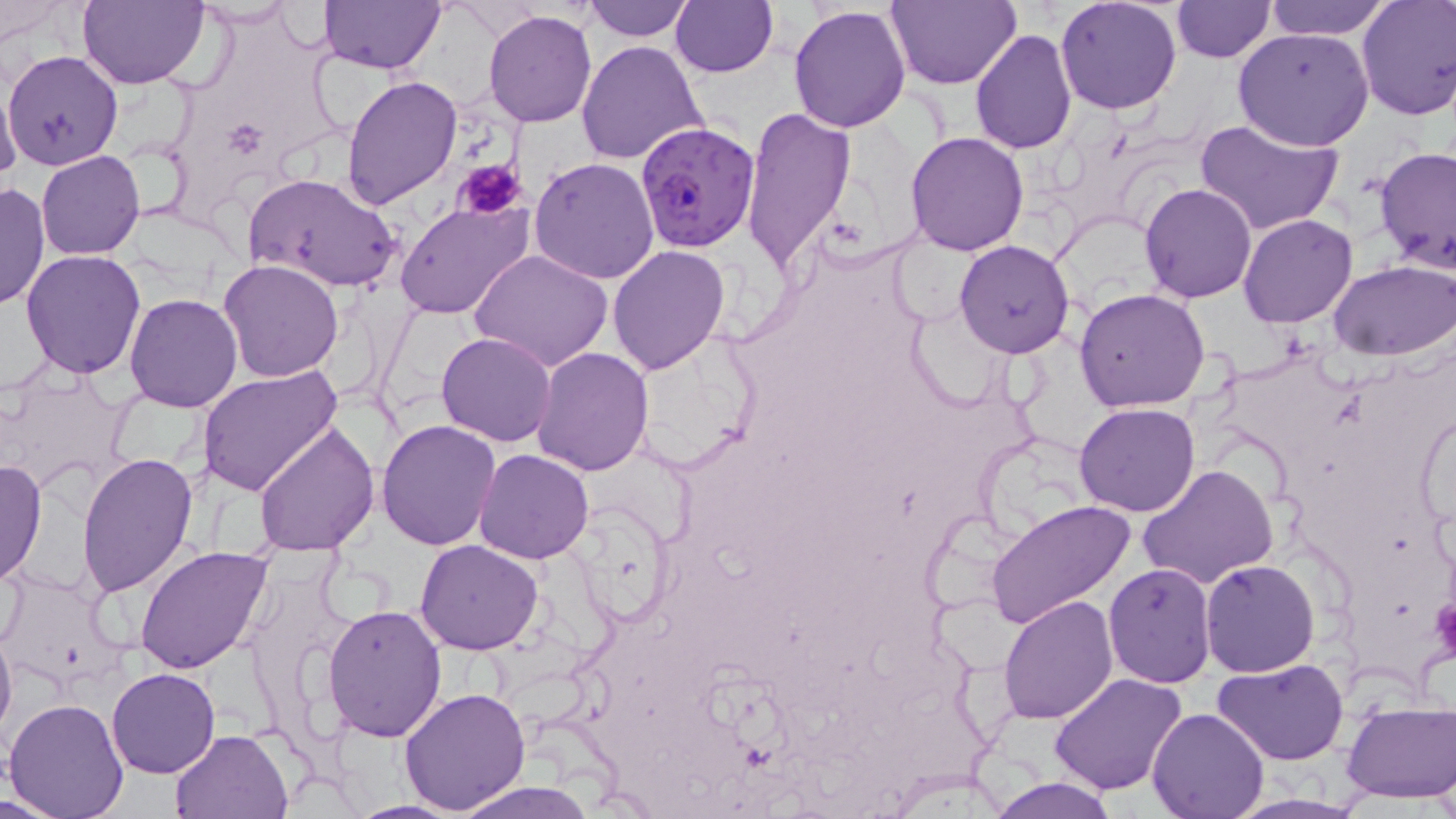

slide-level diagnosis = Plasmodium falciparum
field of view = single
stain = May-Grünwald-Giemsa
platelet locations = approximate bounding boxes as (x1, y1, x2, y2) in pixels: (453, 157, 528, 222), (1431, 596, 1456, 664)
modality = optical microscopy
preparation = thin blood film
image size = 1456×819 pixels
Plasmodium falciparum-infected red blood cell locations = approximate bounding boxes as (x1, y1, x2, y2) in pixels: (635, 120, 761, 249)
uninfected red blood cell locations = approximate bounding boxes as (x1, y1, x2, y2) in pixels: (79, 0, 207, 91), (319, 0, 443, 72), (584, 0, 693, 41), (670, 0, 777, 78), (890, 0, 1021, 88), (1055, 0, 1182, 115), (1268, 0, 1390, 40), (1356, 0, 1456, 120), (1170, 1, 1274, 63), (191, 2, 299, 29), (1, 4, 73, 46), (788, 6, 912, 133), (483, 10, 597, 127), (1233, 28, 1374, 151), (970, 29, 1076, 154), (576, 41, 708, 166), (4, 49, 123, 170), (0, 75, 24, 192), (342, 75, 462, 212), (741, 107, 857, 271), (1195, 118, 1343, 238), (905, 131, 1029, 255), (1375, 147, 1456, 278), (36, 150, 146, 260), (531, 157, 659, 285), (244, 172, 403, 292), (1139, 181, 1258, 302), (0, 182, 49, 312), (397, 202, 532, 319), (1237, 213, 1359, 328), (953, 239, 1075, 359), (608, 245, 729, 374), (21, 249, 147, 377), (469, 249, 613, 371), (219, 260, 345, 382), (1328, 261, 1455, 360), (1075, 288, 1210, 412), (125, 293, 243, 413), (436, 331, 556, 447), (532, 348, 654, 475), (197, 365, 343, 495), (1075, 402, 1201, 516), (1415, 412, 1456, 524), (376, 418, 502, 551), (253, 420, 382, 558), (476, 449, 594, 564), (76, 453, 197, 597), (0, 459, 47, 587), (1137, 464, 1281, 589), (985, 500, 1136, 629), (415, 540, 543, 655), (135, 545, 274, 673), (1200, 559, 1320, 677), (1103, 561, 1217, 686), (999, 593, 1117, 722), (323, 603, 449, 742), (0, 620, 16, 745), (1215, 659, 1349, 766), (107, 668, 220, 779), (1048, 671, 1188, 795), (399, 685, 532, 813), (3, 698, 129, 818), (1341, 700, 1455, 803), (1147, 706, 1269, 818), (170, 729, 292, 817), (984, 777, 1122, 818), (450, 781, 596, 819), (342, 800, 471, 819)
magnification = 1000x